Assess this cell for malaria.
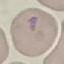
It is uninfected.

Summary:
  - Capture: smartphone camera at the microscope eyepiece
  - Stain: Giemsa
  - Preparation: thin blood smear
  - Image type: automatically extracted cell patch, resized to 64 × 64 pixels